Locate every Plasmodium vivax-infected red blood cell.
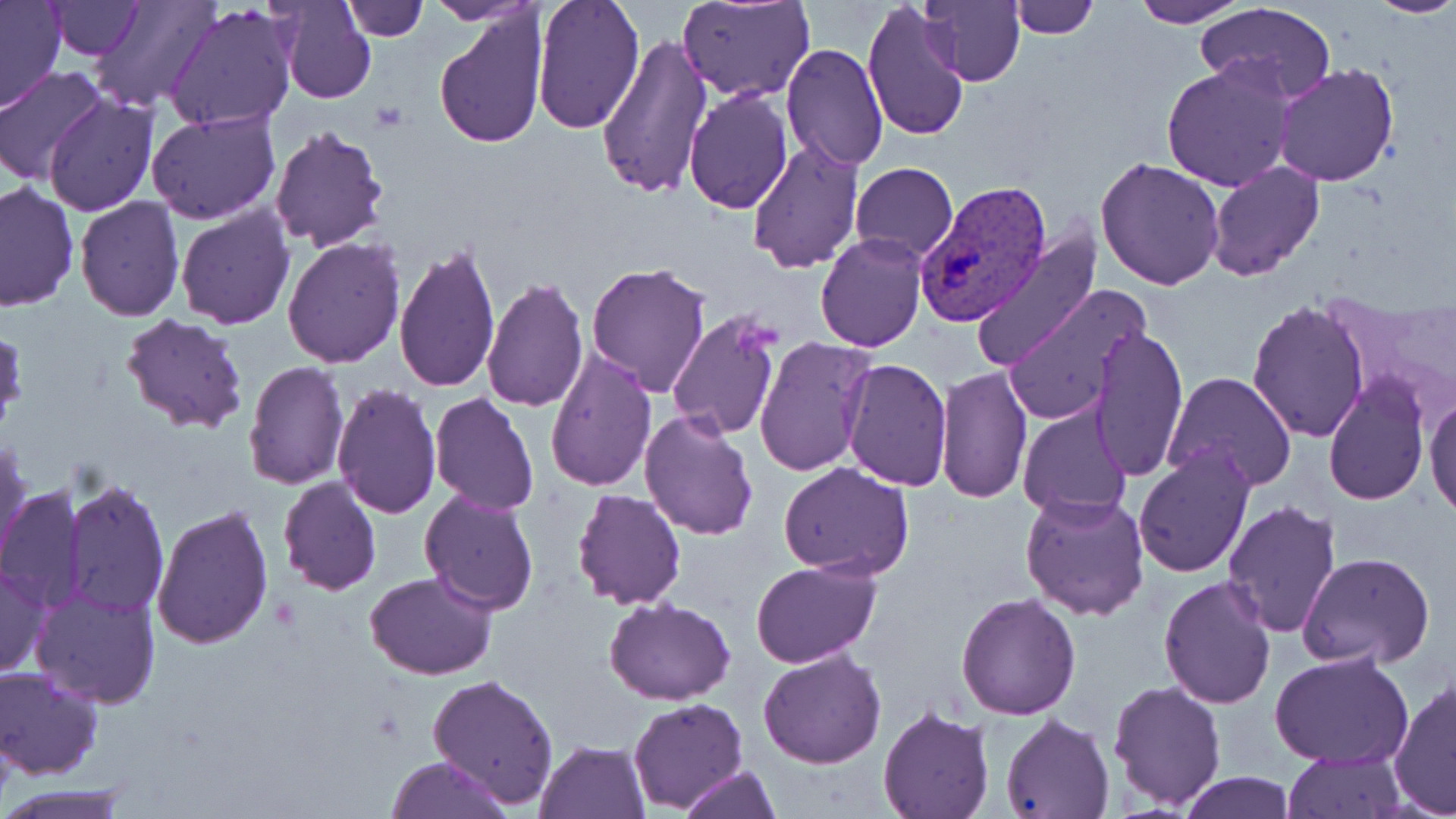
Approximate bounding boxes as (x1, y1, x2, y2) in pixels.
Plasmodium vivax-infected red blood cells: (918, 180, 1052, 328).

Uninfected red blood cell locations: (46, 0, 143, 58), (90, 0, 218, 112), (277, 0, 376, 105), (343, 0, 429, 41), (530, 0, 644, 134), (678, 0, 815, 102), (918, 0, 1026, 87), (1130, 0, 1246, 27), (1365, 0, 1456, 19), (0, 1, 66, 113), (425, 1, 545, 25), (1009, 1, 1098, 38), (1197, 1, 1337, 102), (862, 2, 970, 143), (164, 3, 297, 134), (435, 10, 547, 151), (595, 35, 713, 200), (780, 41, 888, 171), (1161, 59, 1297, 193), (1274, 63, 1400, 186), (0, 68, 109, 184), (683, 87, 793, 212), (44, 93, 158, 216), (145, 109, 280, 226), (268, 124, 389, 253), (747, 138, 864, 274), (1094, 156, 1225, 290), (1207, 160, 1324, 280), (850, 161, 957, 264), (0, 181, 79, 314), (74, 197, 185, 321), (175, 202, 295, 329), (971, 230, 1102, 373), (814, 233, 927, 352), (283, 236, 405, 367), (393, 242, 499, 391), (585, 261, 713, 398), (481, 276, 588, 413), (1001, 284, 1149, 425), (1248, 300, 1371, 444), (118, 312, 250, 437), (667, 313, 785, 442), (1090, 325, 1189, 481), (753, 337, 874, 477), (544, 347, 658, 492), (841, 358, 952, 490), (243, 361, 349, 490), (935, 365, 1033, 504), (1163, 371, 1298, 495), (1323, 375, 1430, 505), (332, 383, 441, 519), (1425, 391, 1456, 520), (429, 392, 539, 514), (1017, 403, 1134, 521), (639, 407, 761, 540), (0, 438, 31, 564), (1133, 444, 1254, 578), (777, 462, 916, 581), (277, 476, 382, 596), (64, 479, 168, 618), (0, 486, 88, 612), (419, 486, 540, 614), (572, 489, 686, 609), (1020, 492, 1150, 621), (1220, 499, 1342, 637), (151, 504, 274, 650), (1297, 552, 1435, 670), (750, 559, 879, 669), (0, 564, 49, 677), (364, 569, 497, 679), (1157, 573, 1278, 709), (31, 587, 161, 708), (955, 592, 1081, 720), (604, 598, 735, 706), (758, 648, 887, 769), (1269, 652, 1413, 769), (0, 667, 103, 781), (427, 673, 559, 807), (1388, 676, 1455, 818), (1106, 678, 1226, 811), (626, 698, 747, 813), (878, 706, 994, 819), (1000, 715, 1114, 818), (0, 722, 16, 809), (534, 739, 650, 819), (1285, 749, 1405, 818), (384, 755, 512, 819), (678, 764, 780, 819), (1178, 773, 1296, 818), (1, 786, 134, 818). Slide-level diagnosis: Plasmodium vivax. Captured at 1000x magnification. Image is 1456×819 pixels. One field of a larger specimen. May-Grünwald-Giemsa-stained preparation. Thin blood film. Light microscopy.